Describe the morphology of the red blood cells.
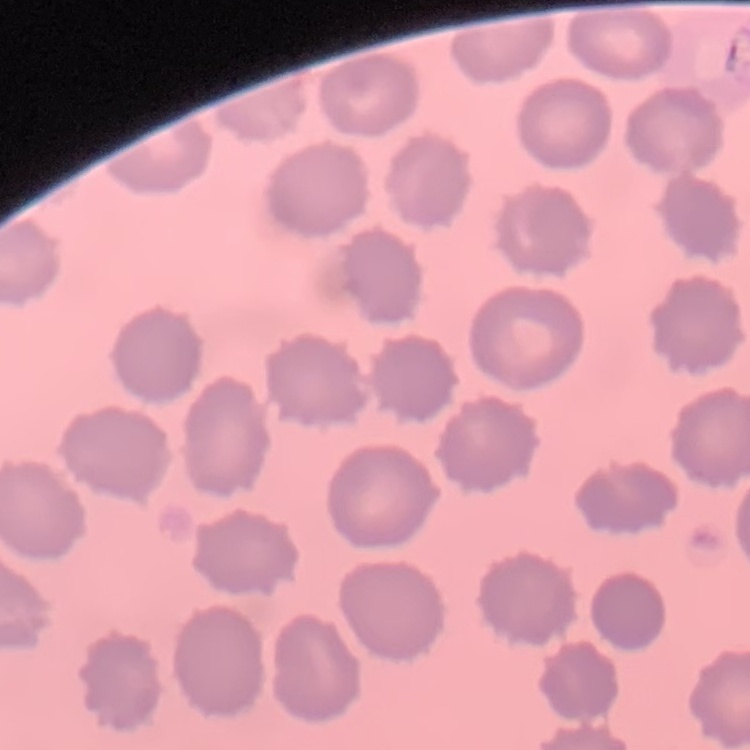
They show no rouleaux formation.

{
  "image_type": "one tile cut from a larger photomicrograph",
  "preparation": "thin peripheral smear",
  "stain": "Field's or Giemsa"
}